Assess this cell for malaria.
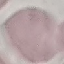

Uninfected.

{
  "image_type": "cell patch, automatically extracted from a larger field of view and resized to 64 × 64 pixels",
  "capture": "smartphone through the microscope eyepiece",
  "stain": "Giemsa",
  "preparation": "thin smear"
}